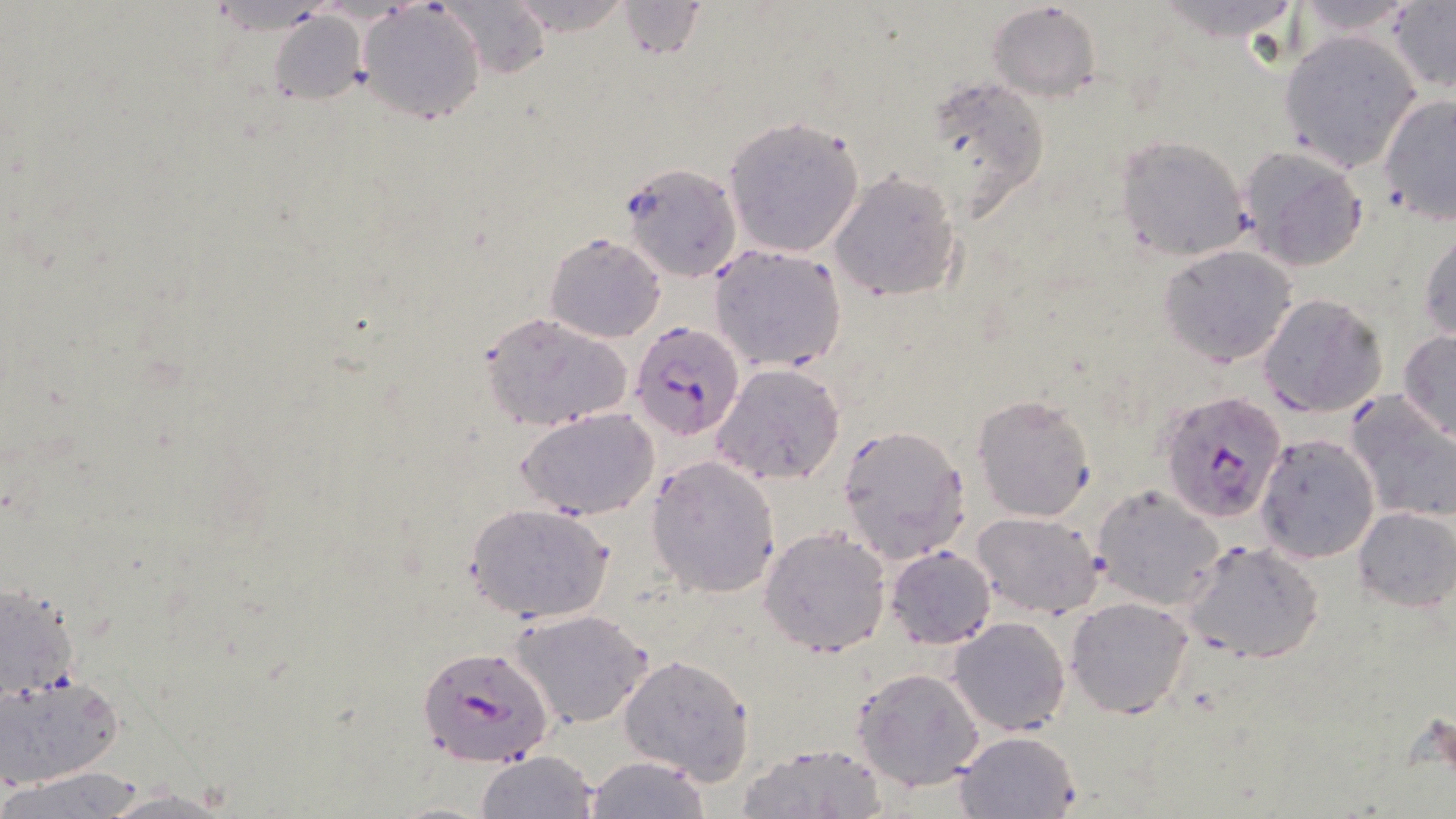

Approximate bounding boxes as [x1, y1, x2, y2] in pixels. Plasmodium falciparum-infected red blood cell locations: [628, 319, 745, 441], [1158, 391, 1288, 523], [421, 650, 559, 771]. Uninfected red blood cell locations: [437, 0, 548, 76], [987, 1, 1102, 105], [1287, 1, 1425, 39], [500, 2, 637, 36], [616, 2, 707, 61], [1150, 2, 1306, 44], [1387, 2, 1455, 92], [358, 6, 485, 124], [266, 12, 368, 108], [1280, 31, 1421, 171], [916, 72, 1053, 220], [1377, 93, 1455, 228], [721, 115, 867, 258], [1113, 134, 1254, 262], [1238, 145, 1369, 272], [617, 163, 741, 282], [830, 172, 963, 303], [1418, 227, 1455, 344], [544, 231, 665, 342], [707, 245, 847, 373], [1159, 245, 1297, 367], [1257, 293, 1386, 418], [478, 311, 634, 432], [1398, 330, 1456, 443], [714, 363, 845, 486], [1345, 391, 1456, 526], [972, 392, 1096, 523], [518, 407, 659, 521], [835, 422, 970, 563], [1254, 433, 1380, 563], [648, 455, 782, 598], [1092, 484, 1224, 610], [462, 501, 615, 624], [1353, 505, 1455, 612], [973, 511, 1104, 619], [758, 526, 891, 658], [1182, 539, 1326, 664], [885, 546, 997, 648], [0, 582, 83, 701], [1066, 598, 1194, 719], [509, 608, 654, 728], [949, 617, 1070, 735], [618, 655, 754, 783], [852, 666, 985, 790], [0, 674, 126, 788], [953, 730, 1080, 818], [737, 742, 888, 818], [477, 751, 600, 819], [583, 756, 713, 818], [4, 769, 147, 818], [99, 787, 235, 817]. Slide-level diagnosis: Plasmodium falciparum. Image is 1456×819 pixels. Single field of view. May-Grünwald-Giemsa-stained preparation. Light microscopy. Thin blood film. Captured at 1000x magnification.